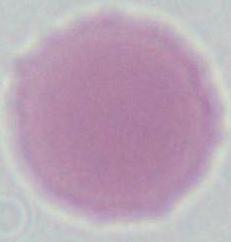
Summary:
  - Modality: photomicrograph
  - Magnification: 1000x
  - Identification: erythrocyte